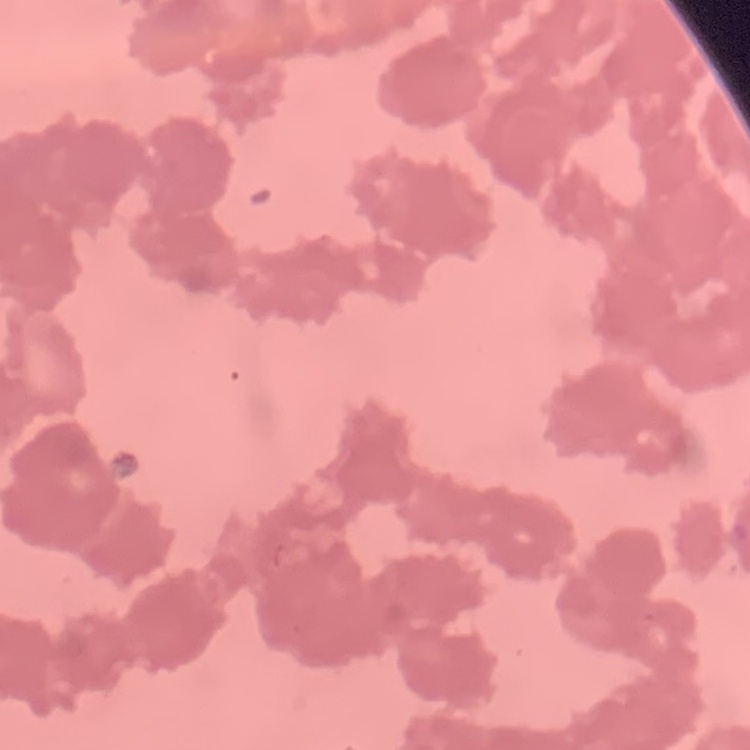
The red blood cells show rouleaux formation. Field's or Giemsa stain. Thin blood smear. One tile cut from a larger photomicrograph.